Locate and identify every blood parasite.
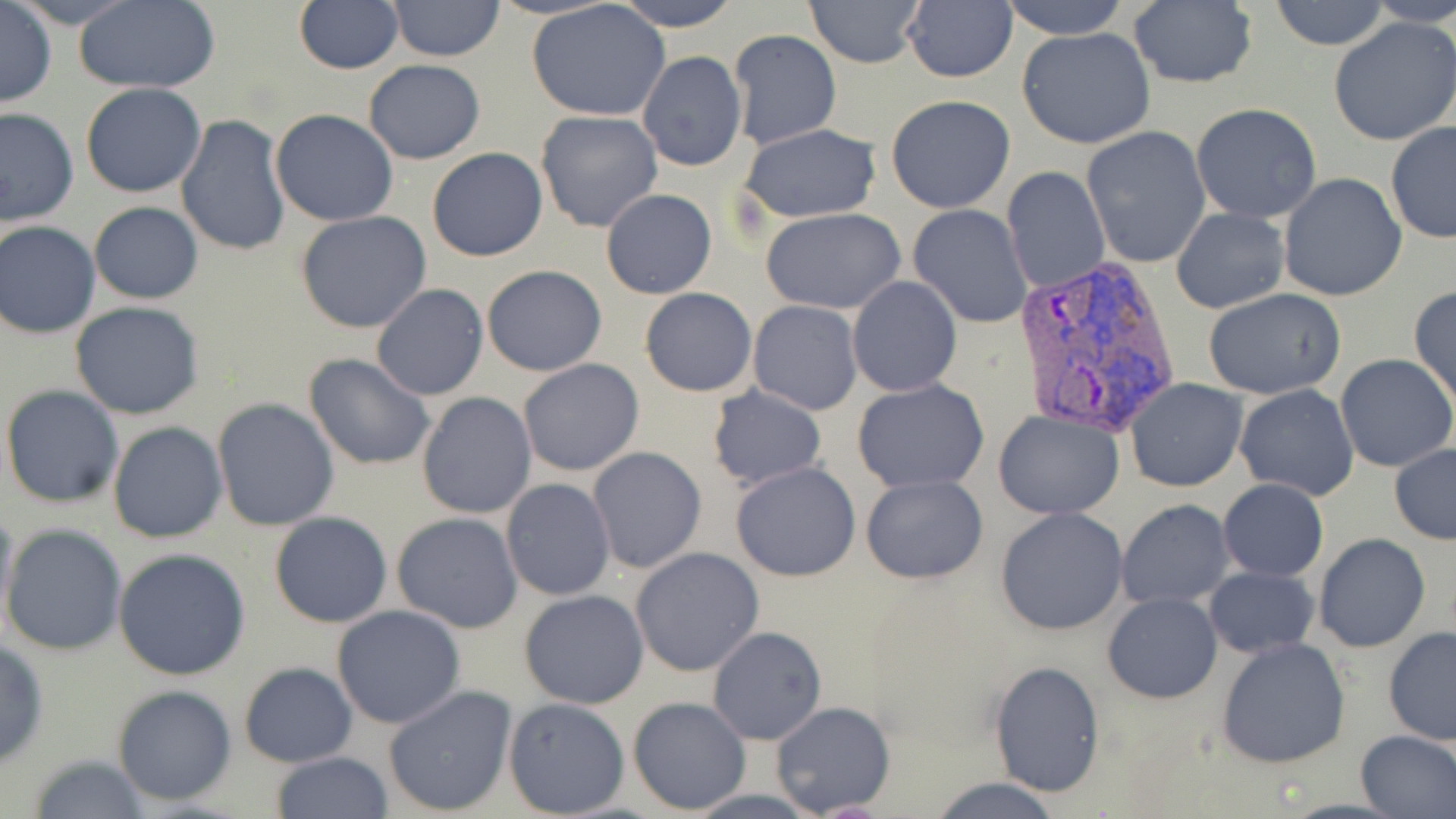
Approximate bounding boxes as [x1, y1, x2, y2] in pixels.
Plasmodium vivax-infected red blood cells: [1015, 259, 1179, 436].
No Plasmodium falciparum, Plasmodium ovale, Plasmodium malariae, Babesia divergens, or Trypanosoma brucei observed.

Summary:
  - Uninfected red blood cell locations: [387, 0, 506, 63], [612, 0, 743, 30], [805, 0, 925, 67], [1000, 0, 1132, 41], [1266, 0, 1391, 50], [73, 1, 221, 93], [293, 1, 404, 74], [527, 1, 671, 122], [1368, 1, 1456, 27], [0, 2, 56, 107], [901, 2, 1018, 83], [1127, 2, 1257, 89], [1328, 15, 1456, 145], [1017, 27, 1156, 149], [727, 30, 843, 150], [636, 50, 747, 172], [364, 59, 485, 165], [80, 82, 207, 198], [884, 94, 1016, 214], [1192, 103, 1323, 224], [0, 106, 79, 228], [536, 109, 663, 233], [270, 110, 399, 225], [176, 114, 292, 257], [1385, 122, 1456, 243], [736, 123, 884, 222], [1082, 126, 1212, 268], [426, 148, 548, 262], [1000, 165, 1111, 293], [1278, 173, 1407, 303], [601, 189, 717, 299], [89, 202, 203, 304], [908, 203, 1032, 328], [759, 207, 906, 313], [1170, 207, 1289, 313], [295, 211, 434, 334], [1, 220, 101, 338], [481, 264, 606, 377], [847, 275, 963, 397], [372, 284, 489, 401], [1409, 286, 1456, 409], [639, 287, 758, 397], [1203, 288, 1348, 399], [70, 301, 204, 419], [748, 301, 862, 416], [303, 353, 436, 473], [1335, 354, 1456, 473], [517, 358, 645, 477], [1125, 377, 1249, 492], [851, 379, 989, 493], [1, 383, 125, 509], [1234, 383, 1361, 501], [707, 385, 827, 492], [416, 391, 538, 519], [212, 398, 340, 532], [993, 410, 1124, 520], [107, 421, 228, 544], [1388, 440, 1456, 544], [588, 446, 706, 574], [730, 461, 861, 582], [861, 475, 987, 584], [499, 478, 616, 602], [1218, 479, 1328, 582], [0, 498, 19, 640], [1116, 499, 1236, 609], [994, 507, 1128, 633], [268, 511, 393, 628], [392, 511, 524, 633], [2, 522, 128, 656], [1313, 533, 1431, 654], [629, 547, 765, 678], [114, 549, 253, 682], [1203, 565, 1319, 658], [519, 590, 650, 709], [1102, 592, 1222, 704], [332, 604, 467, 730], [706, 626, 827, 745], [1382, 628, 1456, 745], [1214, 637, 1353, 769], [0, 638, 50, 768], [987, 660, 1104, 796], [238, 663, 359, 766], [382, 683, 519, 817], [111, 684, 237, 807], [627, 696, 751, 816], [503, 697, 630, 817], [770, 701, 895, 817], [1355, 729, 1456, 818], [268, 751, 395, 819], [27, 752, 152, 819], [928, 777, 1063, 818]
  - Slide-level diagnosis: Plasmodium vivax
  - Preparation: thin blood film
  - Field of view: one of a larger specimen
  - Stain: May-Grünwald-Giemsa
  - Magnification: 1000x
  - Modality: light microscopy
  - Image size: 1456×819 pixels